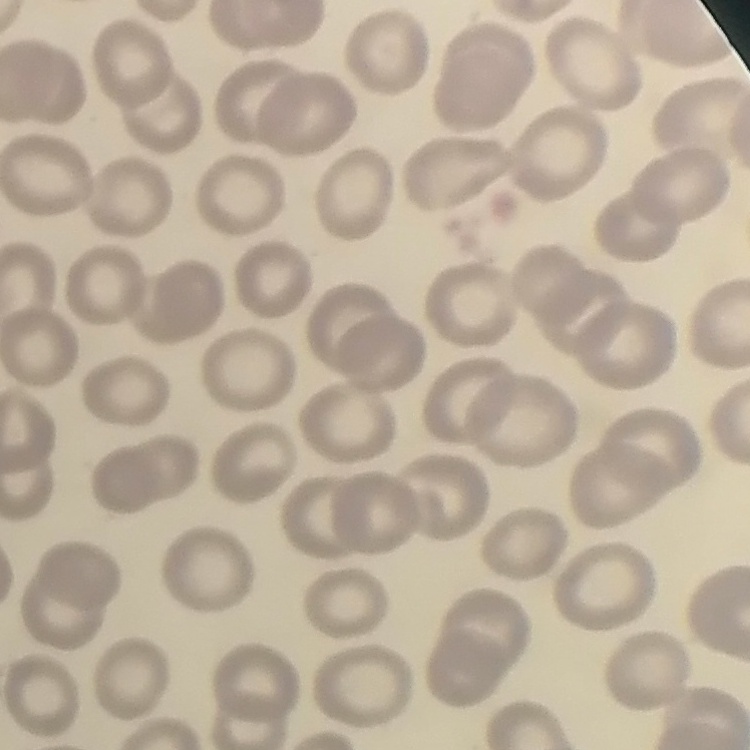

Summary:
  - Red blood cell morphology: no rouleaux formation
  - Image type: one tile cut from a larger photomicrograph
  - Stain: Field's or Giemsa
  - Preparation: thin blood smear